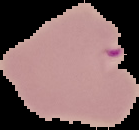

image size = 139×130 pixels
preparation = thin blood smear
malaria status = parasitized
image type = cell region segmented out of the field of view; surrounding area masked to black